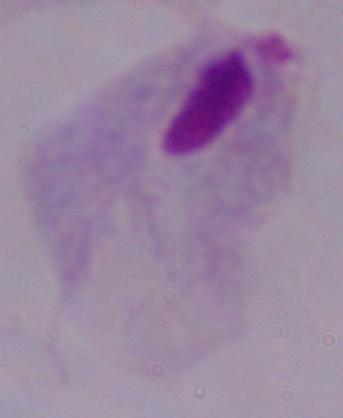

Summary:
  - Magnification: 1000x
  - Identification: trichomonad
  - Modality: photomicrograph